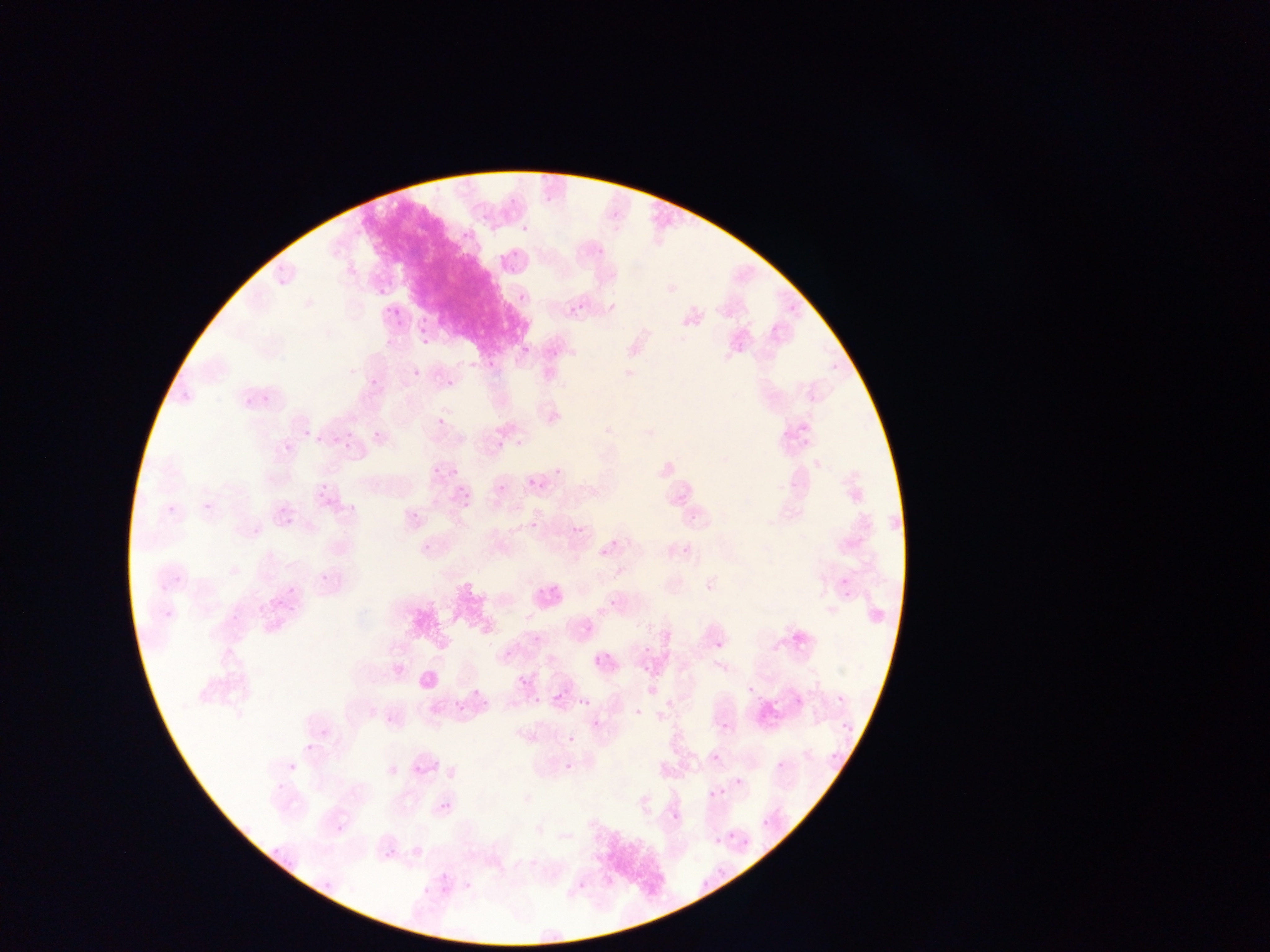

country = Ghana
field of view = single
preparation = thin blood film
capture = mobile-phone photograph through a microscope
image size = 1270×952 pixels
Plasmodium parasite locations = approximate bounding boxes as {left, top, right, bottom} in pixels: {506, 191, 519, 207}, {519, 223, 530, 236}, {458, 228, 476, 245}, {596, 241, 612, 256}, {506, 247, 521, 269}, {518, 292, 527, 303}, {390, 304, 405, 320}, {570, 305, 583, 318}, {412, 310, 436, 340}, {521, 345, 530, 355}, {546, 346, 557, 357}, {471, 350, 484, 368}, {413, 369, 423, 378}, {369, 377, 381, 391}, {446, 378, 456, 388}, {258, 395, 270, 403}, {240, 398, 246, 412}, {790, 414, 823, 442}, {437, 418, 445, 427}, {300, 427, 310, 438}, {371, 427, 388, 449}, {347, 428, 359, 451}, {313, 435, 327, 449}, {497, 441, 505, 449}, {284, 443, 293, 452}, {529, 478, 539, 486}, {459, 480, 473, 505}, {532, 480, 542, 489}, {319, 484, 327, 493}, {497, 485, 506, 495}, {408, 487, 424, 517}, {346, 488, 365, 517}, {204, 502, 213, 512}, {167, 504, 179, 516}, {689, 516, 697, 525}, {284, 518, 293, 527}, {530, 522, 538, 530}, {573, 526, 581, 535}, {422, 542, 434, 555}, {683, 546, 693, 556}, {314, 568, 332, 589}, {535, 572, 565, 600}, {839, 574, 854, 589}, {280, 575, 292, 600}, {606, 581, 620, 611}, {841, 588, 856, 604}, {578, 620, 596, 636}, {533, 635, 541, 644}, {715, 640, 724, 650}, {642, 645, 650, 654}, {504, 651, 512, 659}, {519, 676, 528, 685}, {748, 687, 756, 695}, {472, 688, 481, 698}, {555, 692, 565, 704}, {574, 694, 589, 709}, {836, 694, 846, 704}, {534, 696, 542, 704}, {446, 697, 466, 721}, {635, 708, 644, 717}, {590, 716, 603, 727}, {592, 719, 600, 728}, {721, 722, 730, 731}, {842, 722, 854, 734}, {567, 736, 574, 744}, {305, 744, 314, 753}, {712, 753, 720, 762}, {830, 753, 840, 764}, {777, 760, 785, 769}, {565, 763, 574, 772}, {289, 765, 297, 773}, {734, 777, 743, 786}, {277, 784, 285, 792}, {709, 790, 717, 799}, {441, 803, 452, 815}, {670, 812, 681, 824}, {762, 819, 769, 827}, {335, 822, 347, 834}, {741, 840, 751, 851}, {438, 884, 451, 899}, {421, 885, 430, 895}